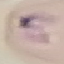

Summary:
  - Malaria status: parasitized
  - Capture: smartphone camera at the microscope eyepiece
  - Image type: automatically extracted cell patch, resized to 64 × 64 pixels
  - Preparation: thin blood film
  - Stain: Giemsa